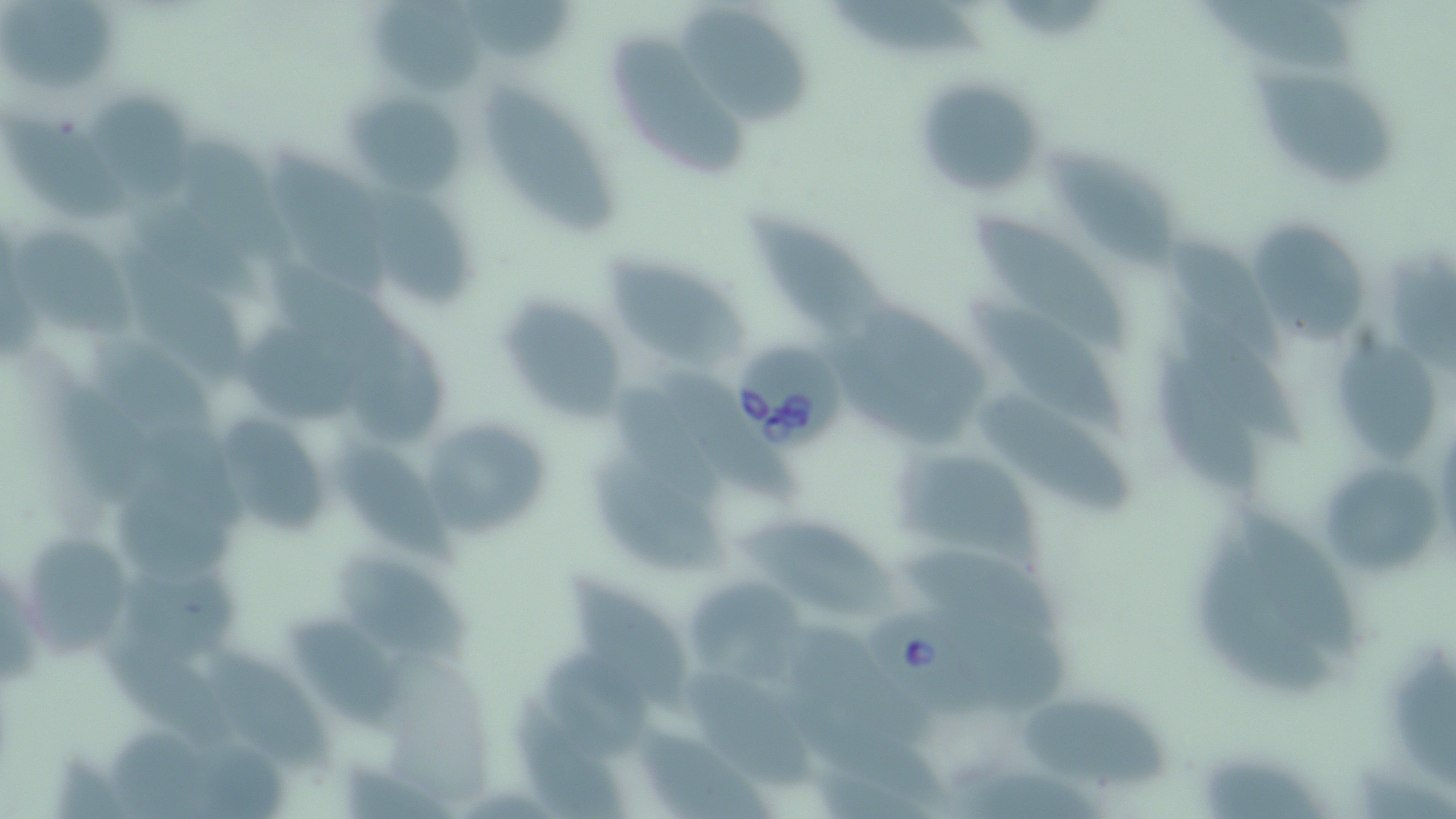
slide-level diagnosis = Babesia divergens
uninfected red blood cell locations = approximate bounding boxes as (x1, y1, x2, y2) in pixels: (462, 0, 579, 62), (1208, 0, 1358, 70), (370, 1, 481, 96), (835, 1, 983, 58), (0, 4, 123, 88), (682, 12, 812, 127), (614, 32, 748, 178), (1253, 64, 1403, 195), (910, 69, 1050, 201), (492, 88, 621, 236), (343, 89, 469, 196), (90, 91, 190, 209), (0, 112, 127, 222), (168, 131, 296, 273), (1047, 145, 1182, 275), (271, 146, 394, 290), (371, 188, 476, 308), (971, 210, 1131, 357), (748, 212, 896, 338), (1255, 225, 1359, 343), (12, 226, 141, 336), (1164, 240, 1284, 353), (119, 241, 252, 378), (1390, 241, 1456, 375), (598, 246, 760, 373), (965, 293, 1126, 436), (499, 298, 629, 422), (346, 301, 452, 450), (1174, 304, 1304, 445), (233, 327, 371, 433), (1334, 330, 1444, 472), (87, 331, 222, 458), (656, 361, 798, 513), (1157, 364, 1271, 501), (981, 393, 1137, 519), (418, 414, 554, 541), (220, 422, 327, 542), (330, 436, 464, 570), (894, 444, 1044, 567), (1314, 453, 1446, 584), (586, 462, 727, 576), (110, 468, 255, 584), (1231, 508, 1361, 654), (731, 515, 904, 621), (20, 533, 133, 658), (1190, 533, 1337, 700), (900, 545, 1070, 647), (328, 552, 481, 670), (114, 556, 232, 656), (567, 574, 693, 705), (693, 588, 812, 692), (276, 617, 417, 732), (95, 633, 257, 755), (201, 642, 335, 778), (1385, 646, 1456, 795), (536, 647, 664, 756), (682, 669, 822, 794), (778, 675, 941, 805), (511, 694, 639, 819), (1019, 696, 1177, 792), (645, 728, 780, 819), (1203, 757, 1338, 819)
magnification = 1000x
field of view = one of a larger specimen
modality = light microscopy
stain = May-Grünwald-Giemsa
image size = 1456×819 pixels
preparation = thin blood smear
Babesia divergens-infected red blood cell locations = approximate bounding boxes as (x1, y1, x2, y2) in pixels: (732, 336, 845, 451), (866, 608, 1010, 714)